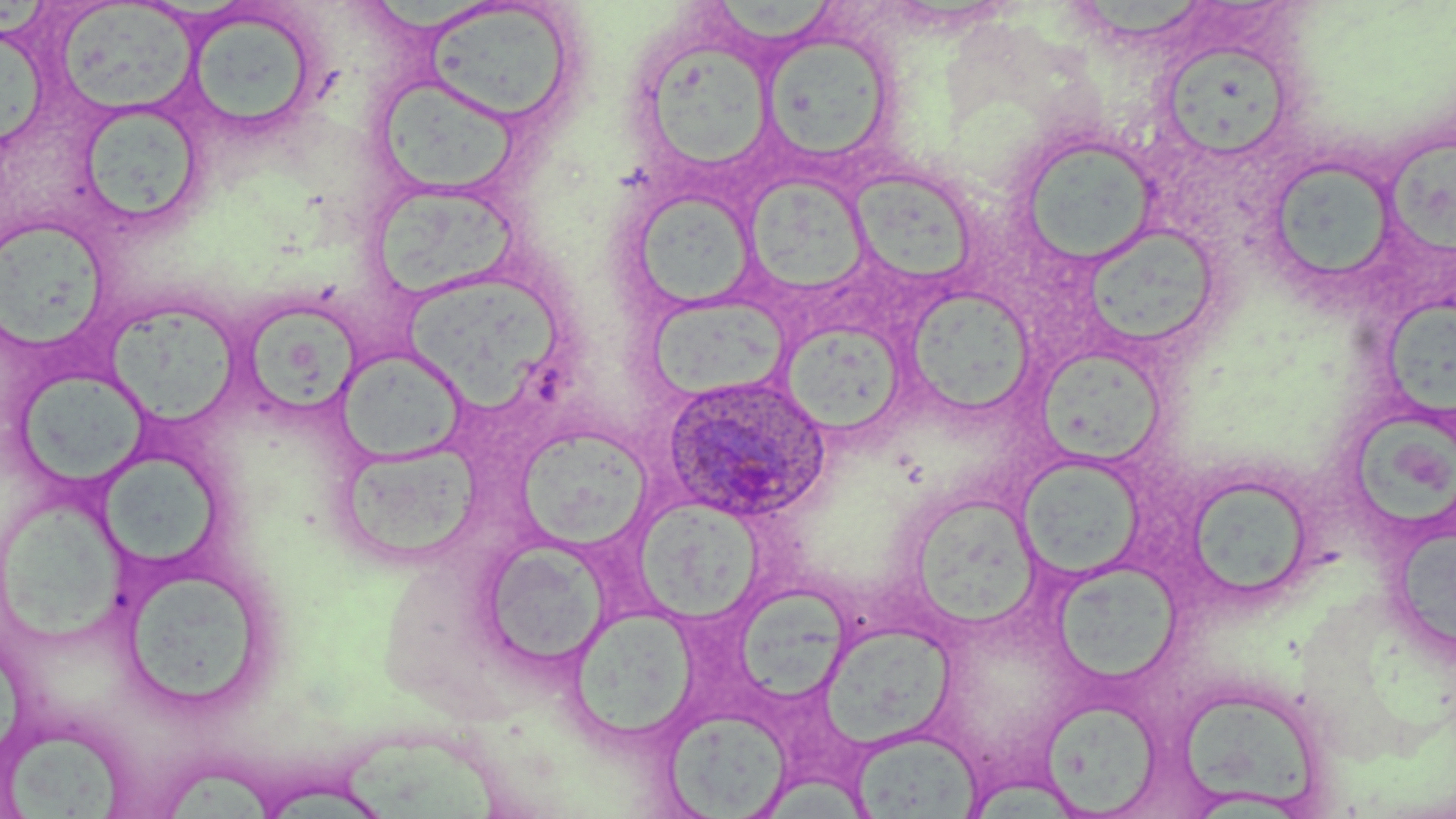

Approximate bounding boxes as (x1, y1, x2, y2) in pixels. Uninfected red blood cell locations: (713, 0, 834, 49), (1083, 0, 1204, 41), (55, 1, 199, 116), (423, 2, 577, 127), (184, 9, 323, 140), (763, 29, 895, 162), (1, 33, 51, 155), (1164, 42, 1284, 163), (645, 45, 775, 170), (383, 80, 519, 198), (72, 101, 208, 231), (1016, 131, 1160, 267), (1388, 141, 1456, 253), (1263, 157, 1401, 289), (851, 171, 983, 283), (748, 172, 874, 289), (632, 188, 759, 310), (377, 190, 520, 301), (0, 219, 111, 350), (1090, 219, 1217, 344), (403, 277, 564, 411), (903, 287, 1037, 417), (646, 293, 790, 402), (1382, 297, 1456, 426), (111, 308, 240, 428), (247, 313, 361, 416), (781, 321, 908, 436), (335, 347, 467, 465), (1039, 348, 1166, 467), (16, 369, 147, 490), (1349, 411, 1456, 526), (515, 425, 653, 551), (342, 439, 481, 558), (1017, 454, 1146, 580), (95, 456, 222, 568), (1181, 473, 1315, 605), (907, 492, 1044, 630), (633, 493, 767, 628), (3, 497, 137, 647), (1397, 528, 1456, 647), (480, 538, 612, 670), (119, 562, 273, 713), (1051, 562, 1185, 684), (737, 582, 857, 704), (569, 605, 700, 744), (822, 624, 959, 753), (1174, 683, 1327, 813), (1041, 698, 1164, 815), (664, 708, 791, 817), (849, 727, 985, 817), (4, 729, 122, 819), (346, 735, 520, 819), (170, 769, 276, 819). Plasmodium ovale-infected red blood cell locations: (661, 374, 832, 523). Slide-level diagnosis: Plasmodium ovale. May-Grünwald-Giemsa-stained preparation. Light microscopy. Image is 1456×819 pixels. One field of a larger specimen. Thin blood smear. Captured at 1000x magnification.